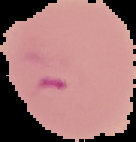
malaria status = parasitized
preparation = thin blood smear
image type = segmented cell region on a black background
image size = 136×142 pixels